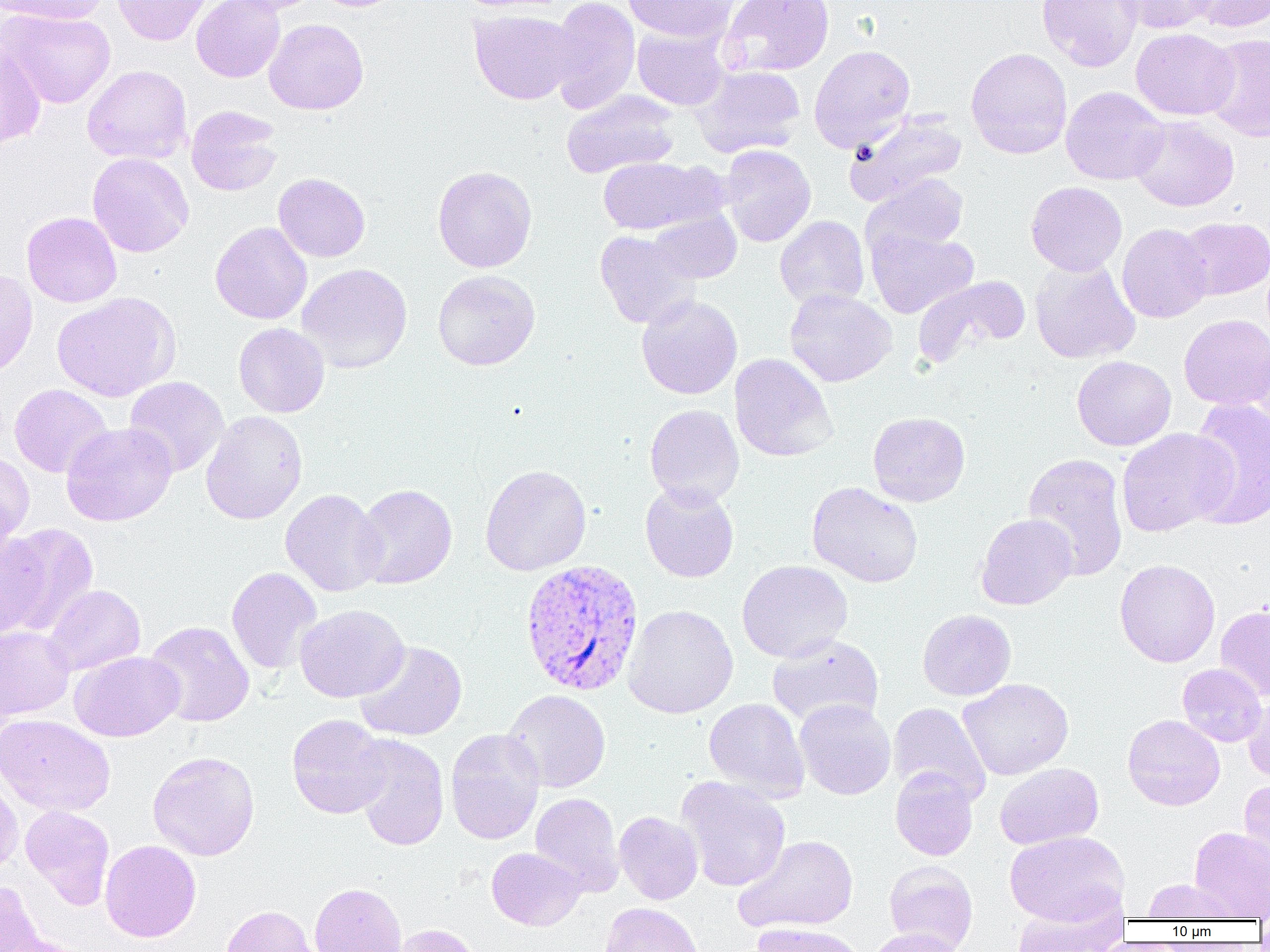
Summary:
  - Coordinate format: approximate bounding boxes as (x1, y1, x2, y2) in pixels
  - Plasmodium vivax-infected red blood cell locations: (520, 559, 645, 697)
  - Uninfected red blood cell locations: (1, 0, 110, 25), (112, 0, 213, 45), (191, 0, 285, 82), (214, 0, 323, 15), (547, 0, 640, 114), (623, 0, 738, 43), (720, 0, 835, 77), (1037, 0, 1143, 71), (1117, 0, 1219, 34), (1187, 0, 1270, 33), (1, 9, 116, 108), (469, 10, 579, 105), (263, 18, 369, 115), (633, 28, 729, 110), (1131, 28, 1239, 120), (1203, 34, 1270, 141), (0, 40, 46, 151), (809, 44, 915, 153), (965, 47, 1073, 159), (82, 65, 192, 165), (694, 66, 805, 157), (1061, 86, 1169, 185), (561, 89, 681, 178), (186, 105, 282, 196), (843, 111, 967, 207), (1130, 115, 1239, 212), (720, 145, 816, 247), (88, 153, 194, 258), (597, 156, 725, 236), (432, 165, 537, 273), (273, 173, 370, 262), (864, 174, 969, 256), (1026, 181, 1127, 276), (648, 208, 741, 284), (21, 211, 122, 307), (775, 215, 869, 310), (1177, 216, 1269, 300), (210, 221, 312, 324), (1117, 223, 1213, 323), (866, 225, 979, 319), (595, 230, 699, 329), (1030, 258, 1140, 364), (297, 263, 412, 373), (0, 268, 38, 379), (432, 269, 540, 370), (912, 275, 1031, 368), (785, 289, 897, 387), (52, 292, 181, 401), (636, 294, 742, 399), (1179, 314, 1270, 410), (234, 323, 329, 417), (1249, 333, 1270, 438), (730, 353, 837, 462), (1072, 355, 1176, 450), (124, 376, 229, 477), (10, 384, 113, 478), (1186, 398, 1270, 529), (644, 404, 744, 507), (201, 410, 308, 525), (868, 411, 970, 506), (61, 422, 177, 526), (1116, 427, 1236, 536), (0, 450, 35, 546), (1023, 453, 1129, 582), (480, 464, 591, 576), (807, 481, 923, 588), (640, 482, 740, 583), (353, 484, 457, 589), (280, 488, 386, 597), (976, 513, 1077, 610), (2, 523, 99, 637), (1, 531, 47, 640), (1114, 559, 1220, 667), (737, 560, 853, 663), (226, 566, 323, 675), (42, 584, 145, 676), (295, 604, 409, 702), (623, 604, 739, 719), (1215, 604, 1270, 701), (917, 609, 1016, 700), (143, 621, 254, 727), (0, 625, 75, 720), (1, 626, 82, 816), (767, 634, 884, 728), (354, 640, 468, 742), (70, 651, 184, 742), (1177, 663, 1267, 747), (957, 678, 1074, 780), (502, 689, 611, 793), (1242, 691, 1270, 782), (704, 698, 809, 801), (794, 699, 896, 800), (888, 702, 991, 805), (0, 714, 115, 817), (287, 714, 392, 819), (1123, 714, 1225, 811), (445, 729, 545, 845), (350, 734, 450, 851), (147, 750, 260, 861), (994, 762, 1103, 850), (890, 767, 979, 861), (0, 774, 23, 877), (676, 776, 791, 892), (1239, 778, 1269, 881), (530, 792, 624, 896), (20, 805, 115, 908), (614, 811, 703, 905), (1189, 826, 1270, 921), (1004, 831, 1128, 925), (734, 834, 859, 934), (100, 840, 201, 942), (486, 847, 586, 931), (883, 860, 978, 952), (1142, 877, 1241, 921), (0, 880, 46, 951), (309, 882, 406, 952), (1011, 898, 1125, 951), (599, 902, 703, 952), (221, 905, 318, 952), (751, 922, 868, 952), (392, 923, 483, 952), (865, 927, 967, 952), (5, 934, 101, 952)
  - Slide-level diagnosis: Plasmodium vivax
  - Magnification: 1000x
  - Image size: 1270×952 pixels
  - Field of view: one of a larger specimen
  - Preparation: thin blood film
  - Modality: light microscopy